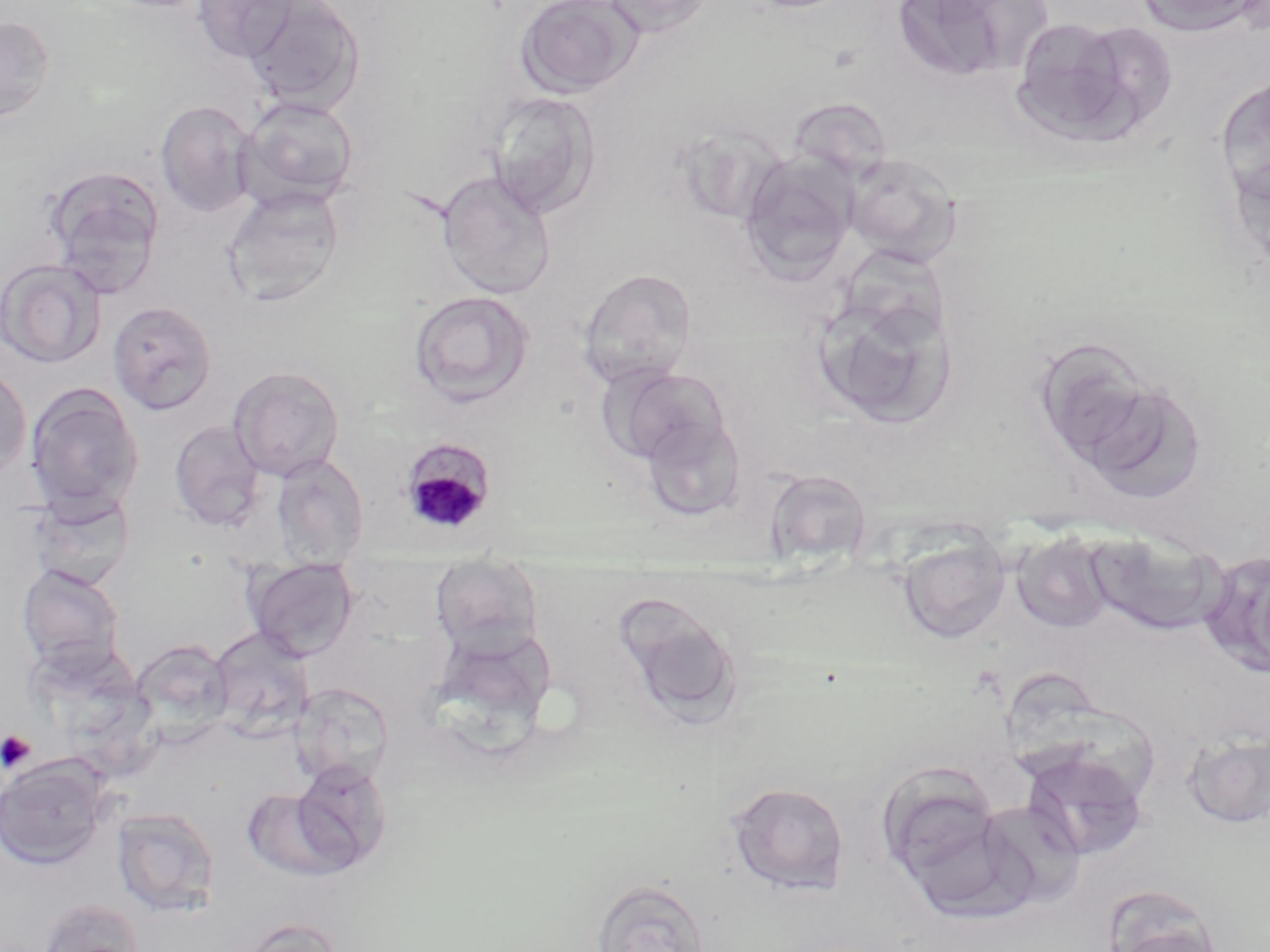

Plasmodium malariae-infected red blood cell locations = approximate bounding boxes as named x1/y1/x2/y2 corners in pixels: (x1=398, y1=436, x2=499, y2=536)
slide-level diagnosis = Plasmodium malariae
platelet locations = approximate bounding boxes as named x1/y1/x2/y2 corners in pixels: (x1=0, y1=730, x2=37, y2=773)
stain = May-Grünwald-Giemsa
uninfected red blood cell locations = approximate bounding boxes as named x1/y1/x2/y2 corners in pixels: (x1=192, y1=0, x2=300, y2=63), (x1=515, y1=0, x2=645, y2=97), (x1=600, y1=0, x2=715, y2=36), (x1=734, y1=0, x2=864, y2=14), (x1=891, y1=0, x2=1048, y2=82), (x1=1134, y1=0, x2=1262, y2=36), (x1=241, y1=1, x2=365, y2=115), (x1=0, y1=15, x2=56, y2=123), (x1=1008, y1=18, x2=1152, y2=146), (x1=1214, y1=74, x2=1270, y2=208), (x1=484, y1=91, x2=600, y2=218), (x1=236, y1=94, x2=360, y2=208), (x1=154, y1=100, x2=258, y2=218), (x1=844, y1=155, x2=961, y2=264), (x1=739, y1=157, x2=857, y2=284), (x1=42, y1=166, x2=165, y2=297), (x1=436, y1=172, x2=556, y2=299), (x1=221, y1=185, x2=345, y2=307), (x1=0, y1=259, x2=107, y2=369), (x1=577, y1=268, x2=698, y2=386), (x1=409, y1=290, x2=535, y2=408), (x1=809, y1=290, x2=954, y2=428), (x1=107, y1=301, x2=218, y2=416), (x1=1031, y1=335, x2=1182, y2=483), (x1=0, y1=361, x2=32, y2=484), (x1=602, y1=364, x2=732, y2=467), (x1=228, y1=366, x2=345, y2=481), (x1=24, y1=383, x2=144, y2=514), (x1=1094, y1=396, x2=1208, y2=505), (x1=639, y1=412, x2=747, y2=521), (x1=169, y1=420, x2=265, y2=531), (x1=271, y1=454, x2=369, y2=563), (x1=765, y1=469, x2=873, y2=567), (x1=25, y1=487, x2=137, y2=591), (x1=1012, y1=532, x2=1115, y2=634), (x1=1089, y1=532, x2=1225, y2=636), (x1=897, y1=533, x2=1011, y2=645), (x1=1198, y1=549, x2=1270, y2=679), (x1=429, y1=560, x2=545, y2=657), (x1=244, y1=561, x2=359, y2=660), (x1=16, y1=564, x2=125, y2=674), (x1=614, y1=595, x2=746, y2=728), (x1=428, y1=624, x2=560, y2=751), (x1=208, y1=628, x2=316, y2=738), (x1=131, y1=639, x2=235, y2=741), (x1=1004, y1=671, x2=1104, y2=780), (x1=290, y1=683, x2=394, y2=787), (x1=1182, y1=729, x2=1270, y2=830), (x1=1020, y1=746, x2=1151, y2=861), (x1=0, y1=757, x2=109, y2=870), (x1=290, y1=760, x2=393, y2=870), (x1=875, y1=761, x2=1003, y2=886), (x1=727, y1=781, x2=850, y2=896), (x1=241, y1=787, x2=352, y2=883), (x1=988, y1=806, x2=1088, y2=909), (x1=111, y1=807, x2=221, y2=917), (x1=591, y1=877, x2=712, y2=952), (x1=1104, y1=894, x2=1228, y2=952), (x1=37, y1=899, x2=145, y2=952), (x1=236, y1=917, x2=345, y2=952)
image size = 1270×952 pixels
field of view = one of a larger specimen
modality = optical microscopy
preparation = thin blood smear
magnification = 1000x